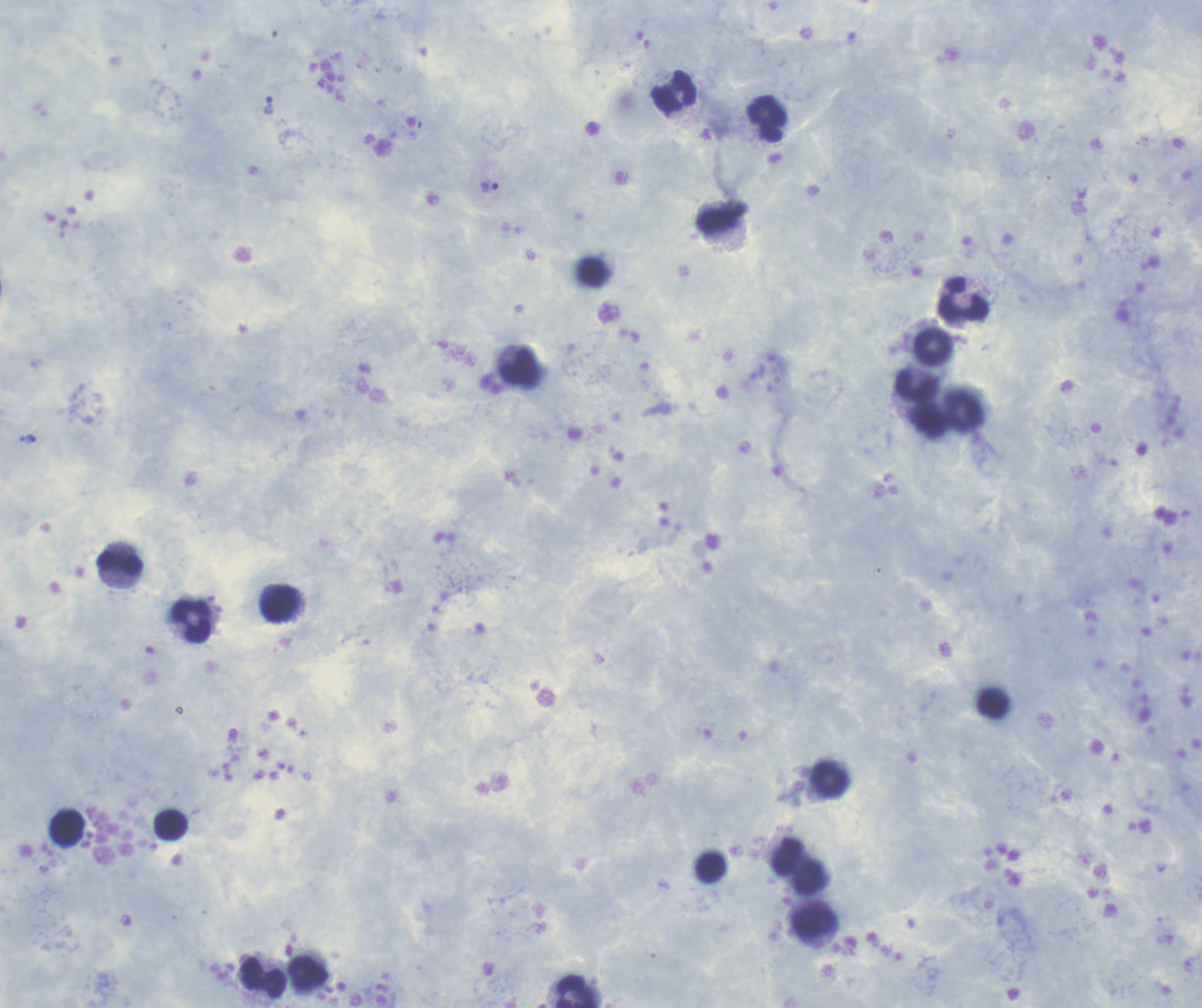
Coloration quality: good. Thick smear of blood. Romanowsky-stained preparation. One field from this slide. Image is 1202×1008 pixels.